Name the cell type shown.
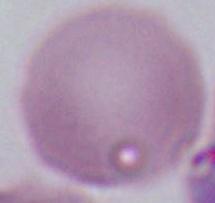

An erythrocyte.

magnification = 1000x
modality = micrograph